Assess this cell for malaria.
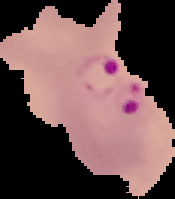
Parasitized.

image_size: 175×199 pixels
preparation: thin blood smear
image_type: segmented cell region with the area outside set to black